Assess the morphology of the erythrocytes.
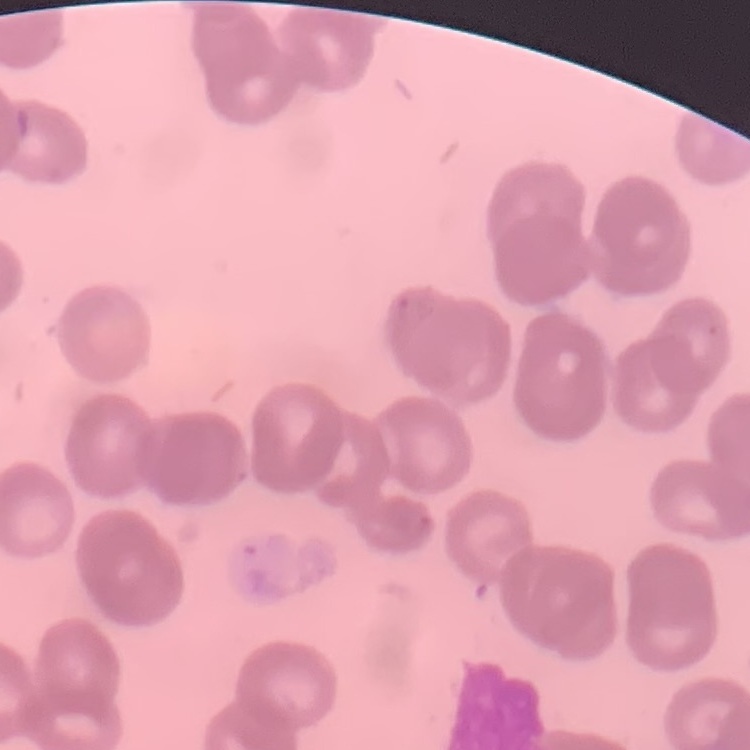

Rouleaux formation.

{
  "preparation": "thin peripheral smear",
  "stain": "Field's or Giemsa",
  "image_type": "square crop of a larger photomicrograph"
}